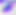 Photomicrograph. Toxoplasma gondii is shown. 400x magnification.